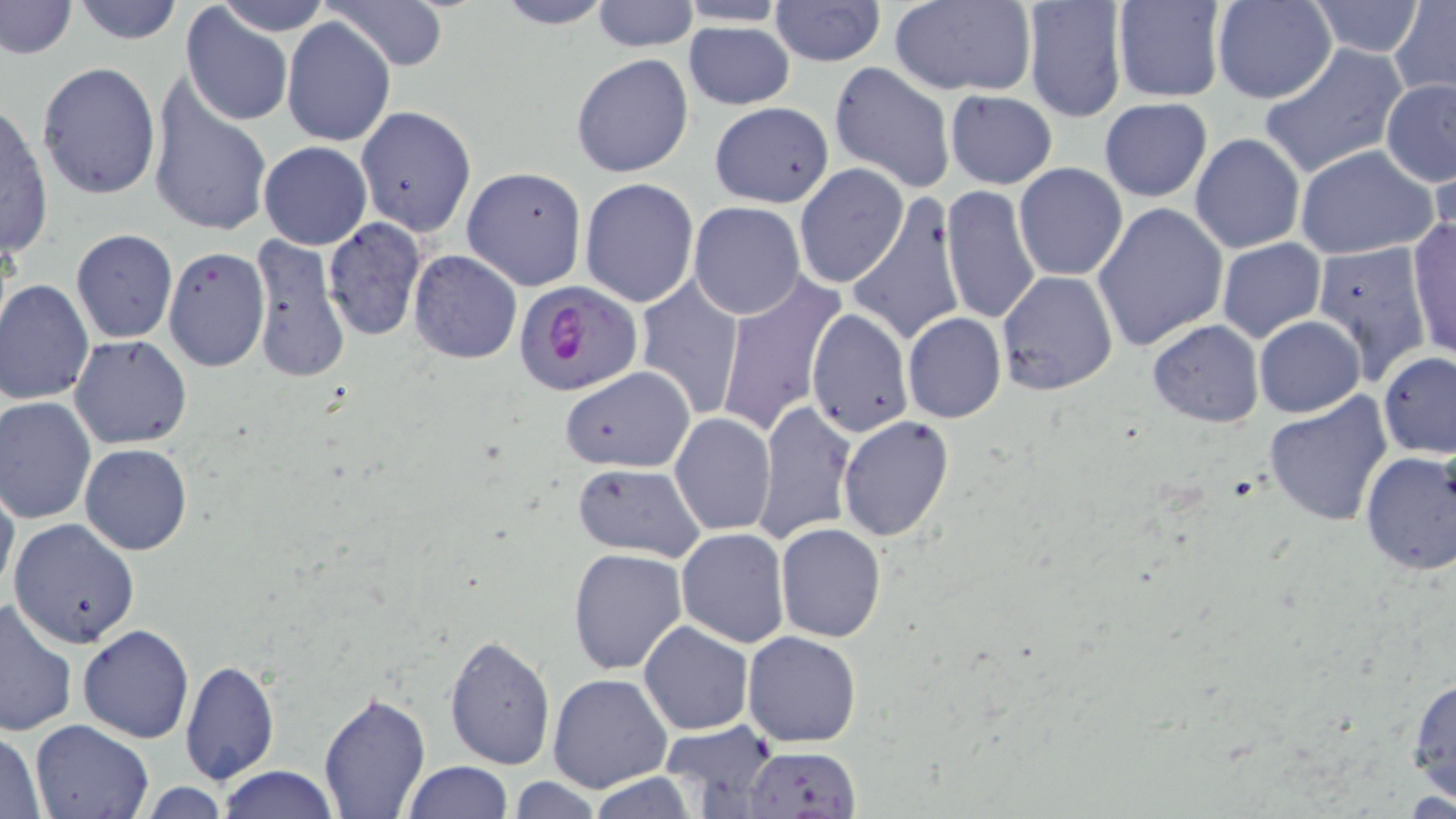 Approximate bounding boxes as [x1, y1, x2, y2] in pixels. Uninfected red blood cell locations: [0, 0, 77, 58], [70, 0, 183, 44], [216, 0, 330, 37], [491, 0, 616, 30], [589, 0, 699, 51], [1212, 0, 1336, 104], [1304, 0, 1427, 57], [328, 1, 450, 71], [769, 1, 884, 67], [888, 1, 1036, 95], [1019, 1, 1127, 124], [1112, 1, 1229, 103], [677, 2, 791, 27], [1391, 2, 1456, 96], [180, 6, 294, 127], [281, 16, 396, 147], [684, 19, 796, 110], [1260, 43, 1409, 179], [570, 53, 695, 177], [37, 61, 161, 200], [828, 61, 956, 195], [147, 79, 272, 237], [1380, 79, 1456, 186], [944, 89, 1057, 189], [1099, 98, 1213, 202], [708, 101, 834, 207], [1, 103, 55, 259], [356, 106, 477, 236], [1189, 132, 1306, 255], [258, 141, 371, 250], [1293, 145, 1439, 261], [794, 163, 908, 287], [1013, 164, 1127, 281], [462, 166, 587, 290], [579, 178, 702, 306], [941, 185, 1041, 327], [845, 193, 967, 347], [1092, 200, 1229, 350], [687, 202, 806, 319], [321, 219, 426, 340], [1405, 219, 1455, 362], [70, 229, 177, 344], [249, 233, 351, 384], [1308, 237, 1432, 379], [1216, 238, 1325, 344], [162, 247, 271, 373], [408, 250, 521, 364], [996, 270, 1118, 395], [715, 273, 845, 439], [634, 275, 747, 421], [0, 279, 95, 405], [806, 307, 913, 438], [903, 313, 1006, 424], [1253, 316, 1365, 418], [1146, 318, 1265, 428], [70, 334, 192, 449], [1377, 351, 1455, 458], [560, 366, 695, 473], [1263, 392, 1394, 528], [0, 396, 97, 524], [755, 399, 856, 543], [669, 412, 777, 536], [837, 416, 955, 541], [79, 443, 192, 556], [1357, 450, 1456, 576], [571, 463, 709, 563], [0, 477, 19, 600], [9, 518, 141, 649], [775, 522, 886, 642], [677, 528, 790, 646], [568, 548, 688, 676], [0, 600, 77, 737], [639, 621, 754, 735], [78, 624, 195, 744], [744, 631, 861, 747], [443, 634, 555, 771], [181, 661, 277, 785], [548, 672, 672, 792], [1406, 674, 1456, 808], [319, 689, 431, 816], [31, 718, 154, 819], [656, 719, 778, 815], [1, 730, 47, 816], [740, 745, 863, 818], [403, 761, 511, 818], [215, 765, 338, 819], [588, 775, 703, 817], [504, 778, 604, 817], [135, 780, 231, 817]. Plasmodium falciparum-infected red blood cell locations: [513, 283, 640, 396]. Slide-level diagnosis: Plasmodium falciparum. May-Grünwald-Giemsa stain. Light microscopy. Thin blood film. One field of a larger specimen. Captured at 1000x magnification. Image is 1456×819 pixels.